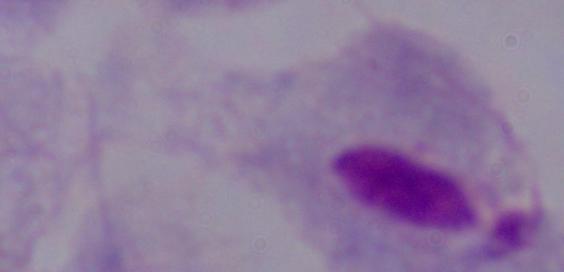

A trichomonad is shown. Photomicrograph. 1000x magnification.